Locate every Plasmodium ovale-infected red blood cell.
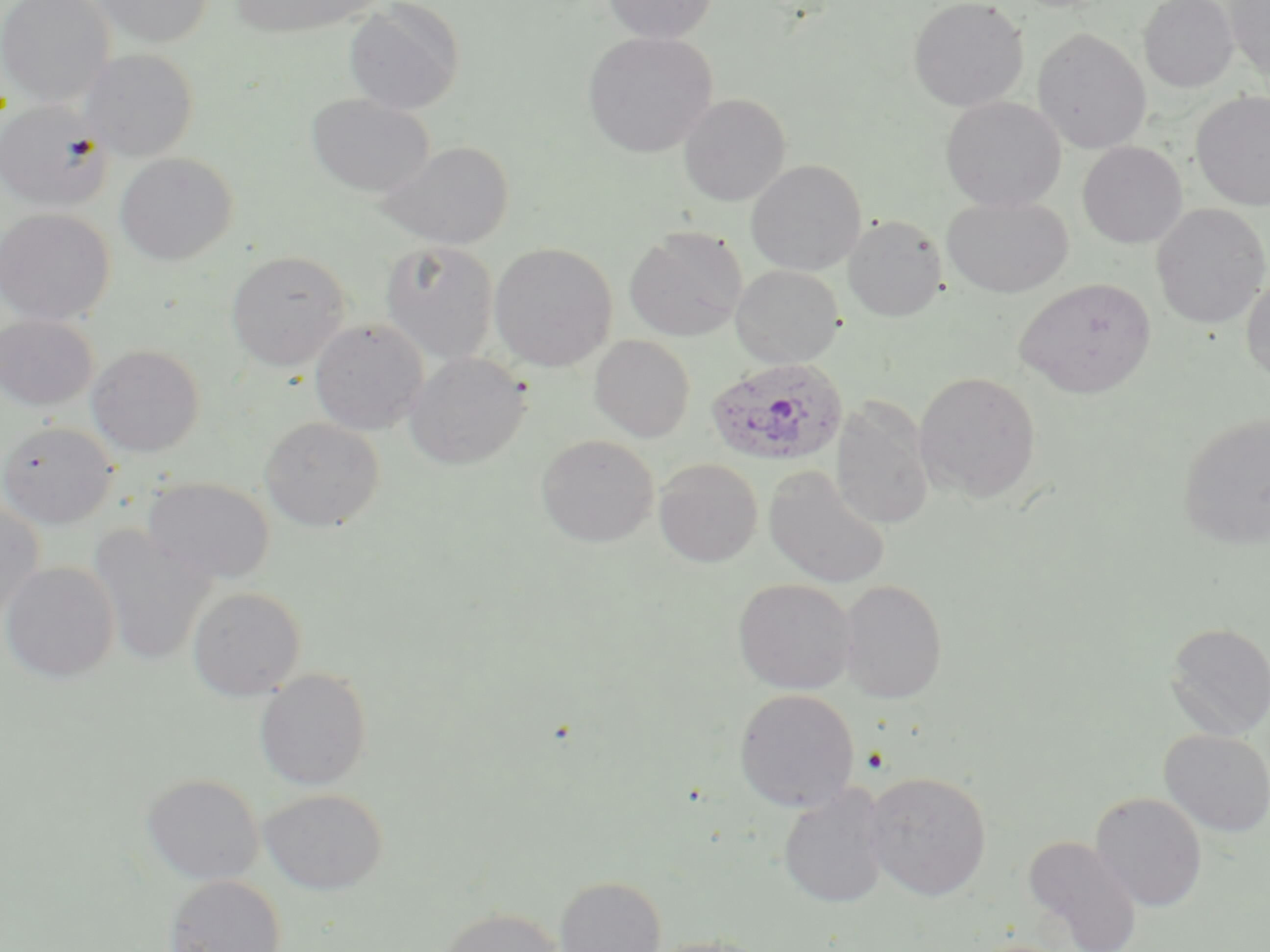
Approximate bounding boxes as (x1, y1, x2, y2) in pixels.
Plasmodium ovale-infected red blood cells: (705, 358, 847, 467).

Uninfected red blood cell locations: (0, 0, 115, 107), (91, 0, 214, 48), (230, 0, 378, 38), (602, 0, 718, 44), (908, 0, 1029, 112), (1139, 0, 1238, 92), (1224, 0, 1270, 82), (343, 1, 465, 115), (1033, 28, 1151, 153), (582, 31, 717, 158), (80, 48, 199, 161), (1191, 91, 1270, 210), (306, 94, 435, 198), (678, 94, 791, 206), (940, 96, 1066, 213), (0, 99, 112, 212), (379, 141, 515, 249), (1077, 141, 1188, 249), (114, 152, 238, 266), (746, 159, 866, 276), (941, 196, 1074, 298), (1151, 204, 1270, 329), (0, 208, 115, 326), (843, 215, 947, 321), (624, 227, 747, 342), (380, 241, 499, 364), (489, 242, 617, 372), (226, 250, 351, 372), (731, 265, 844, 369), (1241, 272, 1270, 385), (1014, 278, 1156, 398), (0, 315, 98, 412), (309, 318, 428, 435), (590, 335, 695, 442), (86, 344, 204, 457), (405, 352, 531, 470), (914, 371, 1041, 503), (832, 404, 933, 530), (1178, 411, 1270, 552), (259, 416, 384, 531), (0, 421, 118, 529), (536, 435, 658, 547), (654, 458, 763, 568), (763, 466, 891, 589), (143, 477, 275, 584), (0, 501, 45, 625), (87, 525, 217, 666), (1, 562, 120, 683), (733, 578, 856, 695), (838, 579, 947, 703), (187, 586, 306, 700), (1164, 622, 1270, 741), (254, 669, 373, 790), (734, 688, 860, 812), (1159, 729, 1270, 837), (864, 772, 991, 901), (142, 773, 264, 885), (778, 784, 890, 909), (259, 788, 388, 895), (1090, 791, 1208, 912), (1022, 834, 1143, 952), (163, 875, 286, 952), (555, 875, 666, 952), (439, 908, 563, 952), (644, 935, 772, 952). Slide-level diagnosis: Plasmodium ovale. Thin blood film. Captured at 1000x magnification. May-Grünwald-Giemsa stain. Light microscopy. One field of a larger specimen. Image is 1270×952 pixels.